State which parasite is depicted.
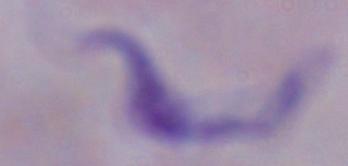

This is a trypanosome.

magnification: 1000x
modality: photomicrograph